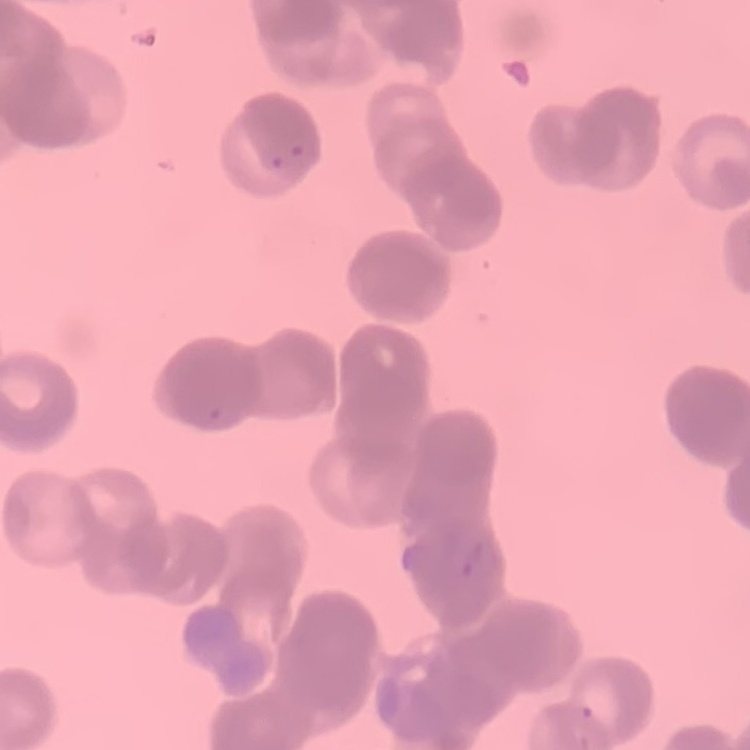
Summary:
  - Red blood cell morphology: rouleaux formation
  - Image type: one tile cut from a larger photomicrograph
  - Preparation: thin blood film
  - Stain: Field's or Giemsa